State which parasite is depicted.
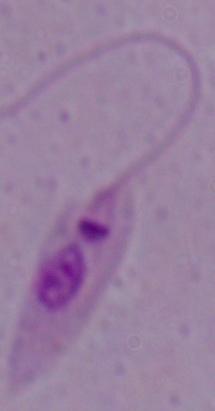

Leishmania.

{
  "magnification": "1000x",
  "modality": "photomicrograph"
}